Comment on the morphology of the erythrocytes.
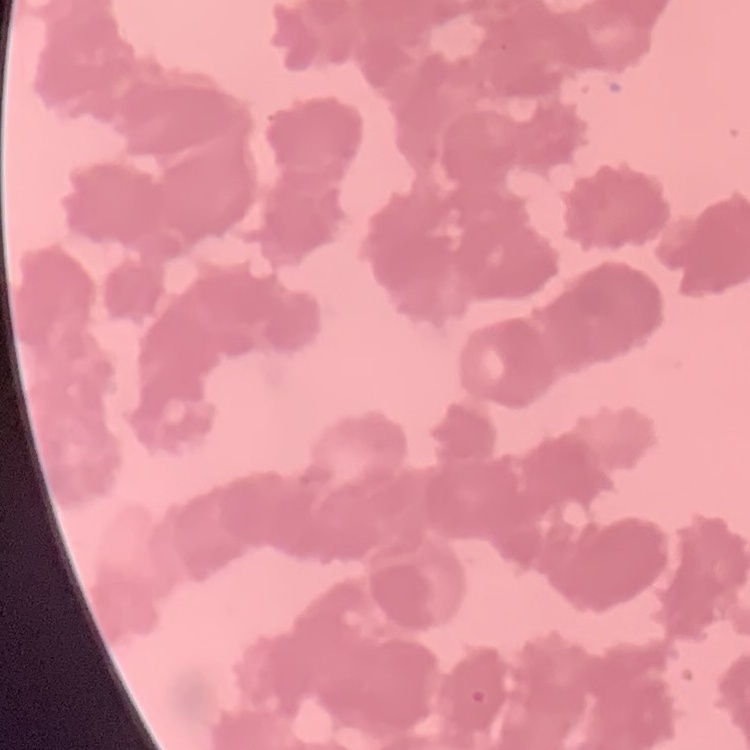

Rouleaux formation.

Summary:
  - Image type: square crop of a larger photomicrograph
  - Stain: Field's or Giemsa
  - Preparation: thin blood film